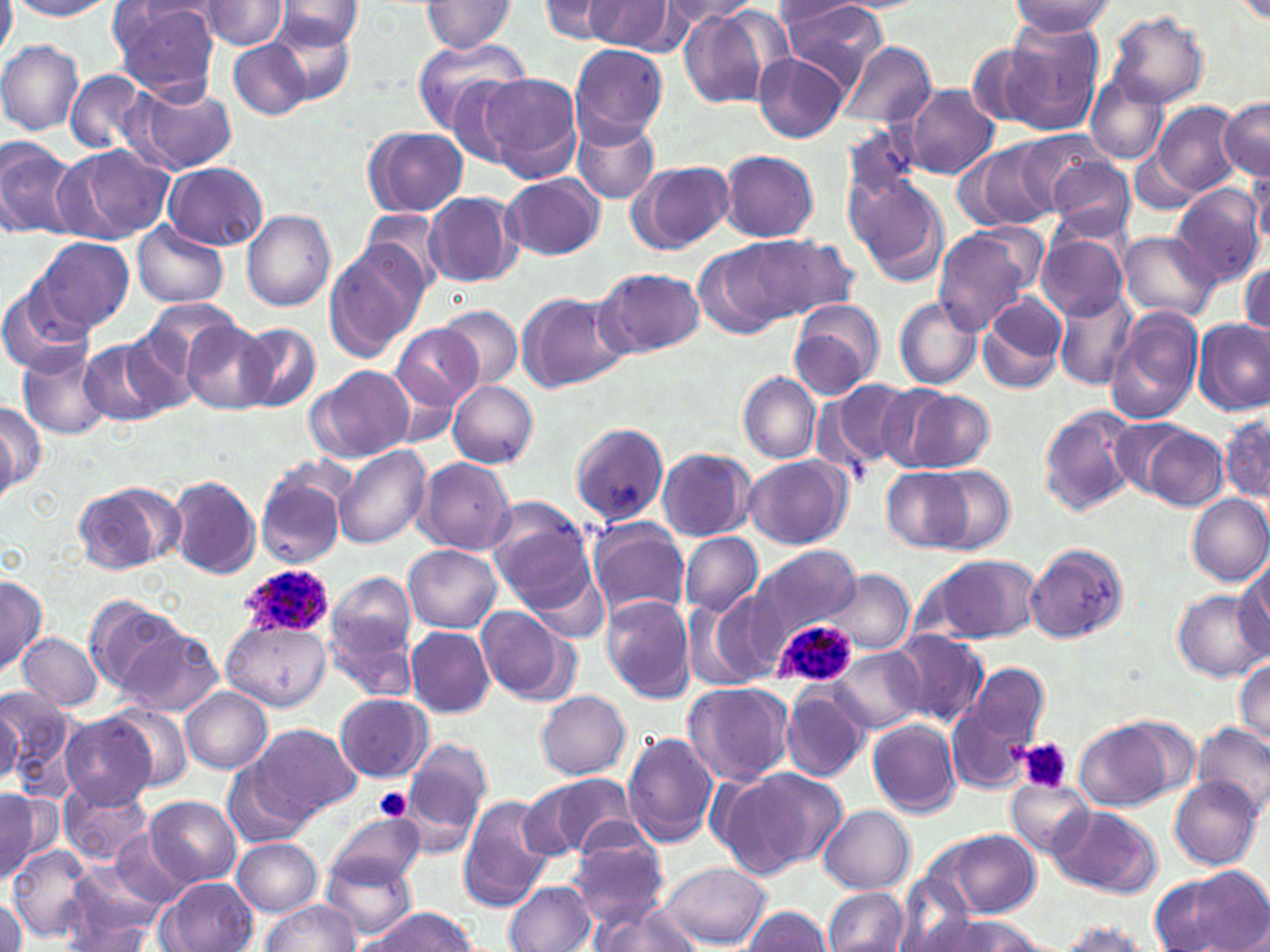
slide_level_diagnosis: Plasmodium ovale
stain: May-Grünwald-Giemsa
platelet_locations: 'approximate bounding boxes as (x1,y1)-(x2,y2) corner pairs in pixels: (1020,737)-(1072,794), (374,787)-(412,822)'
image_size: 1270×952 pixels
field_of_view: one of a larger specimen
uninfected_red_blood_cell_locations: 'approximate bounding boxes as (x1,y1)-(x2,y2) corner pairs in pixels: (0,0)-(16,61), (108,0)-(223,102), (540,0)-(630,44), (585,0)-(687,55), (777,0)-(890,85), (1235,0)-(1270,26), (8,1)-(114,19), (194,1)-(290,51), (273,1)-(364,50), (419,1)-(518,54), (661,1)-(760,26), (1009,1)-(1114,39), (678,4)-(791,111), (1106,11)-(1209,109), (264,18)-(359,103), (1000,22)-(1107,132), (411,36)-(530,132), (228,38)-(313,120), (0,39)-(84,134), (837,41)-(935,129), (569,46)-(667,142), (754,53)-(848,144), (64,69)-(152,155), (1086,72)-(1169,165), (474,73)-(581,180), (125,82)-(237,175), (902,85)-(1001,181), (1218,98)-(1269,180), (1152,101)-(1242,198), (571,115)-(659,206), (841,124)-(920,208), (363,125)-(469,218), (1014,132)-(1113,217), (0,134)-(79,240), (963,140)-(1058,230), (62,144)-(175,243), (717,149)-(819,243), (1128,149)-(1201,212), (1043,154)-(1138,242), (628,160)-(733,255), (162,161)-(270,251), (1249,165)-(1270,255), (843,170)-(950,287), (502,175)-(605,261), (1171,185)-(1267,289), (424,191)-(522,288), (361,209)-(449,297), (242,210)-(336,311), (133,222)-(228,309), (933,229)-(1030,335), (1119,230)-(1218,323), (1037,232)-(1127,320), (754,234)-(858,317), (34,236)-(133,334), (697,239)-(806,341), (324,241)-(428,362), (1238,261)-(1269,335), (596,267)-(704,357), (0,279)-(97,376), (1053,290)-(1137,390), (979,291)-(1069,392), (517,292)-(629,393), (894,297)-(982,389), (789,299)-(884,399), (138,300)-(243,382), (438,308)-(523,389), (1105,308)-(1203,425), (1193,319)-(1269,417), (182,321)-(276,413), (236,323)-(319,412), (391,323)-(482,416), (78,339)-(172,427), (17,347)-(112,440), (310,366)-(414,463), (738,372)-(821,464), (816,377)-(920,475), (447,381)-(539,467), (888,387)-(998,473), (0,402)-(44,493), (1037,404)-(1142,517), (1220,410)-(1268,505), (570,420)-(666,525), (1135,423)-(1228,511), (334,445)-(432,549), (656,448)-(755,543), (743,455)-(852,549), (417,458)-(516,555), (254,464)-(349,568), (926,466)-(1015,555), (881,469)-(975,552), (167,474)-(262,580), (73,481)-(180,574), (1185,493)-(1270,586), (487,499)-(597,611), (586,518)-(691,620), (679,532)-(763,617), (754,544)-(862,641), (405,546)-(502,633), (1024,546)-(1129,644), (921,553)-(1042,644), (1233,564)-(1270,659), (831,569)-(914,655), (325,573)-(418,671), (0,576)-(46,677), (1172,590)-(1264,681), (686,592)-(784,691), (88,595)-(183,693), (601,595)-(696,702), (476,605)-(577,705), (220,619)-(333,709), (405,627)-(495,716), (118,628)-(226,718), (889,630)-(989,728), (19,633)-(103,712), (829,647)-(923,733), (1233,659)-(1270,750), (961,662)-(1049,756), (682,682)-(794,786), (780,685)-(868,783), (1,687)-(76,792), (181,687)-(273,773), (535,690)-(631,780), (947,690)-(1039,796), (333,694)-(433,782), (0,696)-(22,790), (109,703)-(195,792), (59,714)-(156,809), (869,719)-(962,818), (1074,719)-(1174,812), (1192,723)-(1270,816), (253,724)-(360,819), (623,732)-(721,847), (403,736)-(493,832), (221,759)-(316,850), (720,765)-(847,877), (529,774)-(640,860), (1168,775)-(1261,870), (1008,779)-(1093,857), (59,782)-(153,870), (0,790)-(50,880), (456,792)-(559,912), (146,796)-(243,888), (1048,804)-(1160,896), (819,807)-(914,894), (328,812)-(424,888), (112,829)-(189,904), (948,830)-(1041,920), (565,831)-(670,929), (232,837)-(323,917), (7,845)-(95,942), (322,854)-(420,941), (662,863)-(770,947), (59,868)-(167,952), (1151,868)-(1268,952), (161,876)-(258,952), (503,881)-(595,952), (821,887)-(909,952), (0,897)-(26,949), (262,900)-(359,952), (592,903)-(703,952), (742,906)-(832,951), (362,907)-(480,951), (909,914)-(1045,950), (1051,922)-(1157,951)'
magnification: 1000x
preparation: thin blood film
plasmodium_ovale_infected_red_blood_cell_locations: 'approximate bounding boxes as (x1,y1)-(x2,y2) corner pairs in pixels: (238,563)-(334,638), (768,616)-(859,691)'
modality: light microscopy